Locate and identify every blood parasite.
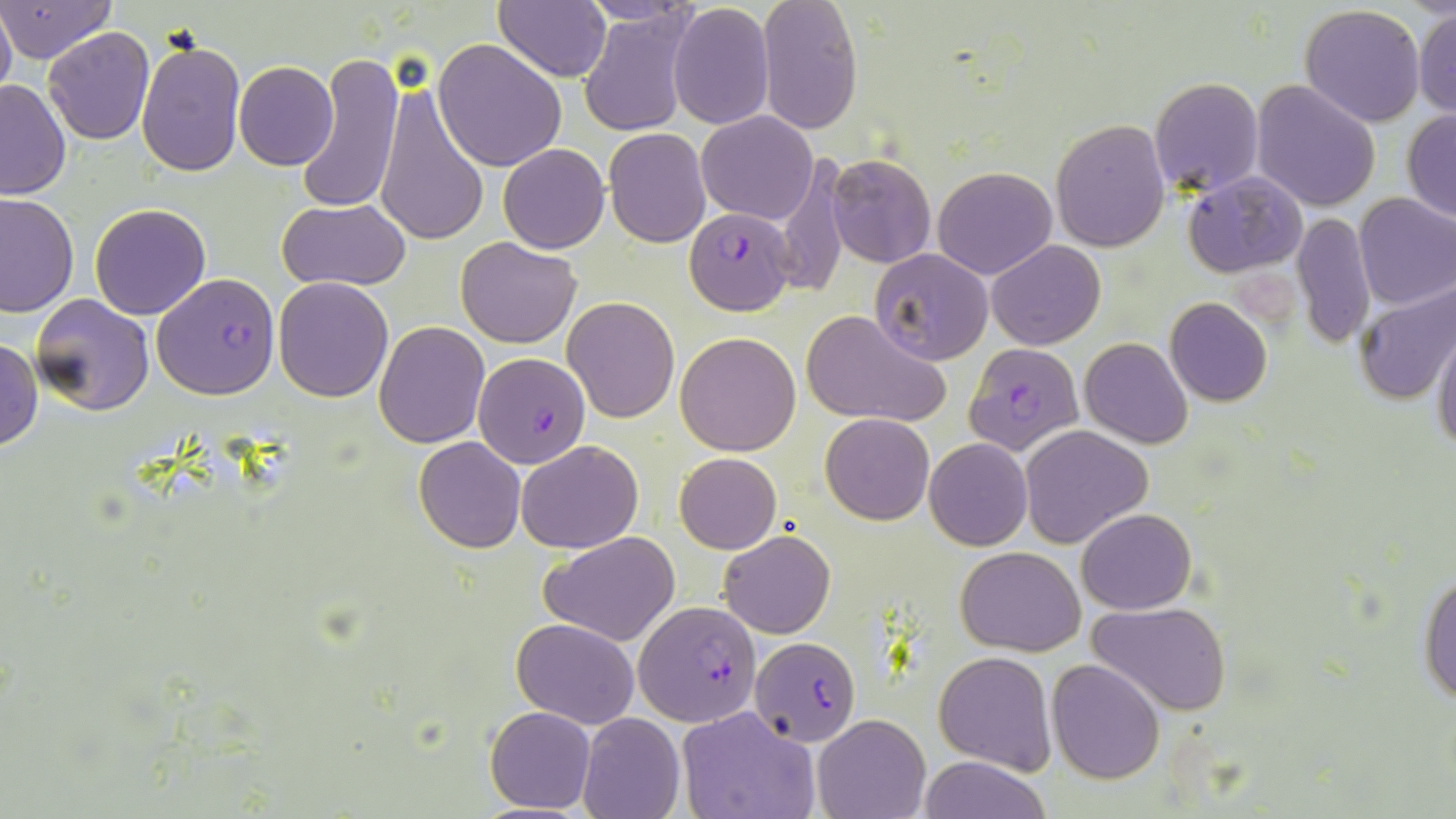
Approximate bounding boxes as (x1,y1)-(x2,y2) corner pairs in pixels.
Plasmodium falciparum-infected red blood cells: (686,207)-(796,315), (152,273)-(280,400), (965,343)-(1088,461), (474,350)-(592,468), (639,600)-(763,724), (750,637)-(859,743).
No Plasmodium ovale, Plasmodium malariae, Plasmodium vivax, Babesia divergens, or Trypanosoma brucei observed.

slide-level diagnosis = Plasmodium falciparum
stain = May-Grünwald-Giemsa
platelet locations = approximate bounding boxes as (x1,y1)-(x2,y2) corner pairs in pixels: (1229,270)-(1302,334)
preparation = thin blood smear
magnification = 1000x
field of view = one of a larger specimen
uninfected red blood cell locations = approximate bounding boxes as (x1,y1)-(x2,y2) corner pairs in pixels: (496,0)-(614,83), (576,0)-(703,27), (757,0)-(863,136), (0,1)-(115,63), (667,4)-(774,130), (1299,4)-(1427,127), (0,5)-(15,105), (1413,6)-(1456,120), (579,8)-(695,137), (43,27)-(156,146), (136,38)-(246,177), (432,39)-(566,172), (297,47)-(406,213), (234,60)-(338,170), (1149,76)-(1263,197), (0,79)-(71,199), (1252,80)-(1381,211), (375,83)-(490,249), (1401,110)-(1456,222), (697,111)-(817,223), (1049,118)-(1172,252), (604,128)-(712,248), (497,142)-(610,253), (825,154)-(937,269), (771,156)-(850,300), (932,166)-(1057,279), (1184,171)-(1308,276), (1353,192)-(1456,310), (1,193)-(78,318), (279,198)-(410,293), (90,203)-(211,319), (1291,211)-(1376,352), (455,236)-(582,348), (987,240)-(1105,350), (869,249)-(995,366), (273,278)-(393,402), (1352,279)-(1456,406), (31,293)-(155,416), (563,295)-(679,424), (1164,297)-(1273,407), (800,308)-(950,428), (374,321)-(490,448), (1431,322)-(1456,455), (675,332)-(802,456), (1080,337)-(1192,450), (0,338)-(42,453), (821,412)-(934,525), (1020,424)-(1153,549), (413,438)-(525,553), (924,439)-(1033,551), (515,440)-(642,554), (675,452)-(781,553), (1078,508)-(1196,614), (540,530)-(680,645), (719,530)-(835,639), (956,547)-(1085,655), (1418,565)-(1456,708), (1087,602)-(1231,716), (511,618)-(640,729), (934,650)-(1056,773), (1046,659)-(1166,784), (485,707)-(597,814), (679,707)-(822,819), (578,712)-(685,819), (812,715)-(929,819), (919,755)-(1049,819)
modality = optical microscopy
image size = 1456×819 pixels